Give the extent of all Plasmodium ovale-infected red blood cells.
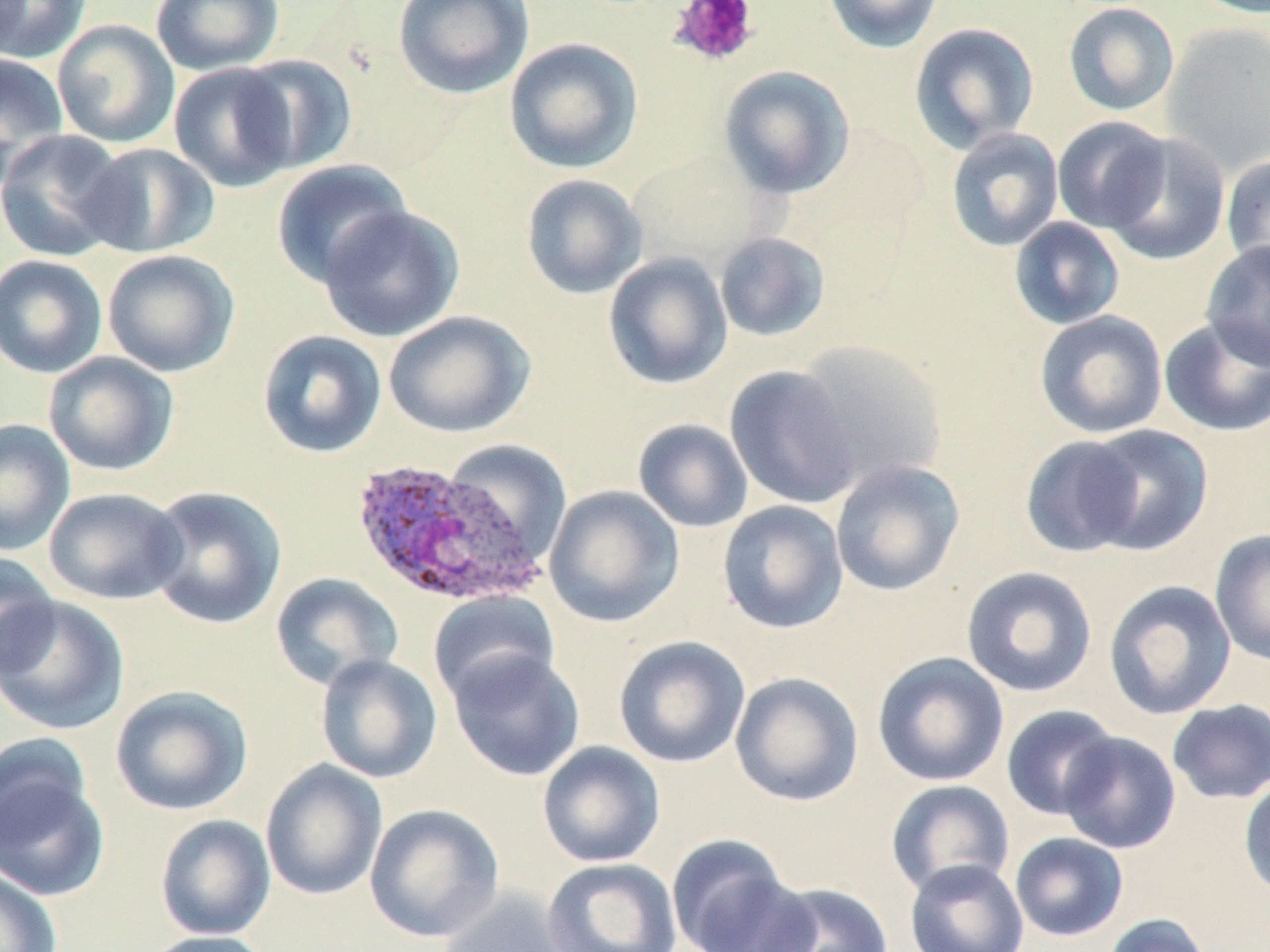

Approximate bounding boxes as (x1, y1, x2, y2) in pixels.
Plasmodium ovale-infected red blood cells: (348, 457, 547, 607).

Platelet locations: (670, 0, 759, 68). Uninfected red blood cell locations: (1, 0, 91, 63), (150, 0, 284, 75), (392, 0, 534, 99), (823, 0, 945, 53), (1189, 0, 1270, 19), (1063, 2, 1180, 117), (52, 19, 180, 149), (909, 22, 1040, 153), (1162, 22, 1270, 176), (504, 37, 644, 174), (0, 53, 69, 183), (233, 54, 358, 175), (169, 63, 298, 192), (718, 65, 855, 199), (1052, 116, 1171, 234), (0, 128, 132, 262), (946, 128, 1064, 252), (1103, 133, 1230, 266), (78, 142, 219, 258), (1221, 153, 1270, 278), (270, 159, 413, 288), (520, 173, 648, 300), (317, 203, 465, 343), (1009, 217, 1126, 330), (714, 231, 831, 343), (1201, 240, 1270, 371), (102, 249, 240, 377), (603, 252, 733, 390), (0, 254, 108, 379), (383, 310, 535, 439), (1034, 310, 1168, 439), (1158, 317, 1270, 437), (256, 329, 388, 459), (791, 338, 949, 490), (43, 352, 179, 477), (725, 364, 862, 510), (633, 418, 754, 533), (0, 419, 76, 556), (1082, 424, 1214, 556), (1019, 434, 1146, 558), (441, 438, 572, 566), (830, 459, 965, 598), (143, 485, 287, 630), (543, 485, 685, 628), (43, 487, 188, 605), (717, 500, 849, 634), (1210, 528, 1270, 666), (0, 552, 60, 679), (960, 566, 1098, 697), (271, 573, 404, 691), (1103, 579, 1237, 720), (429, 590, 560, 708), (0, 595, 131, 735), (613, 636, 751, 769), (446, 647, 586, 782), (872, 652, 1010, 787), (314, 654, 443, 784), (730, 672, 864, 806), (110, 685, 253, 816), (1167, 698, 1270, 804), (1000, 704, 1120, 821), (1058, 731, 1181, 854), (537, 741, 666, 867), (0, 744, 111, 905), (260, 759, 388, 901), (1238, 774, 1270, 900), (885, 779, 1015, 898), (364, 803, 505, 943), (155, 813, 276, 941), (1009, 832, 1129, 942), (666, 834, 805, 952), (543, 857, 682, 952), (904, 859, 1029, 952), (0, 868, 62, 952), (756, 882, 894, 952), (437, 890, 577, 952), (1101, 913, 1213, 952), (139, 930, 275, 952). Slide-level diagnosis: Plasmodium ovale. Image is 1270×952 pixels. One field of a larger specimen. May-Grünwald-Giemsa-stained preparation. Optical microscopy. 1000x magnification. Thin blood film.